Locate every uninfected red blood cell.
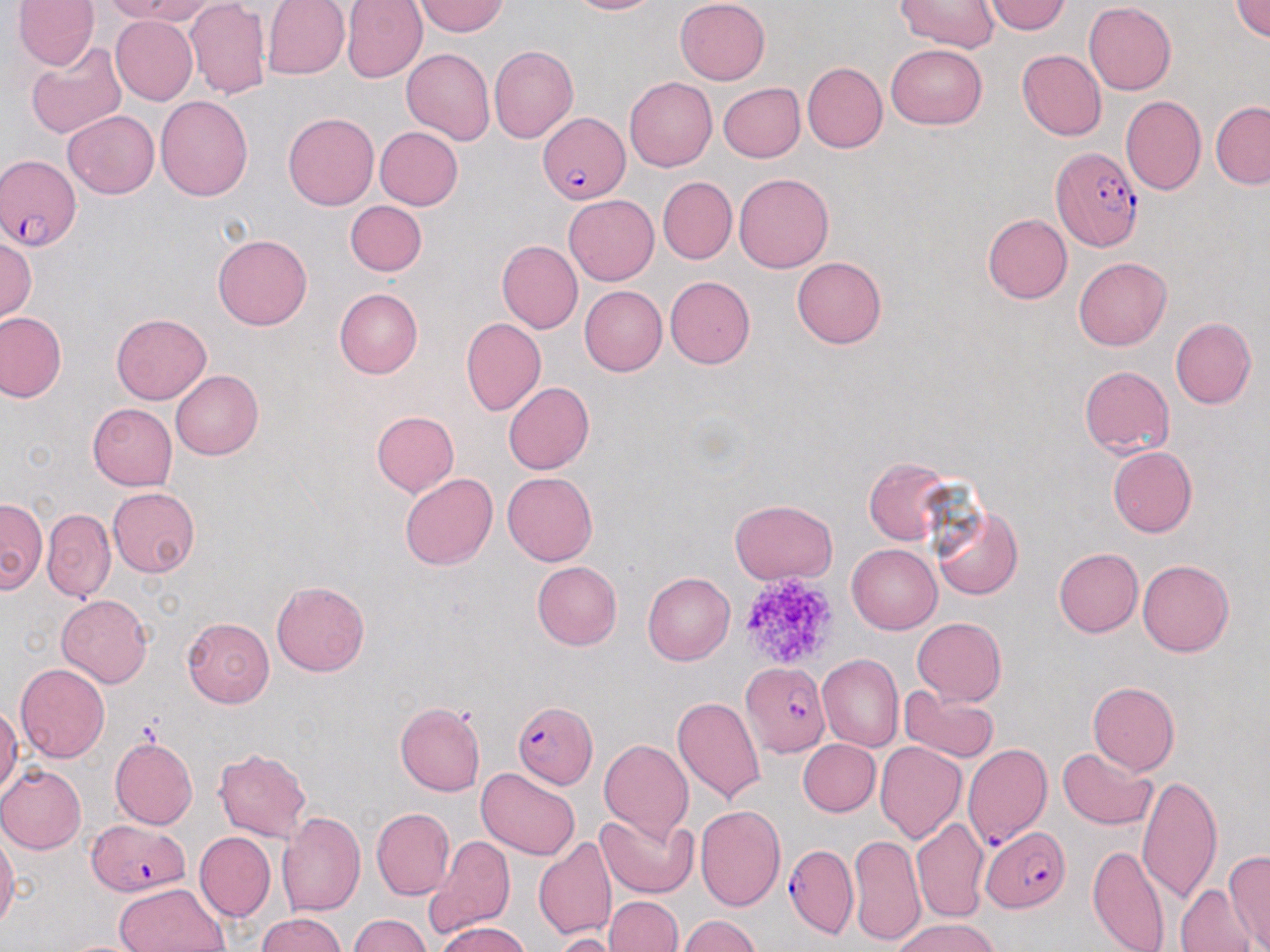
Approximate bounding boxes as (x1, y1, x2, y2) in pixels.
Uninfected red blood cells: (12, 0, 100, 69), (101, 0, 208, 24), (262, 0, 350, 80), (342, 0, 427, 83), (568, 0, 658, 15), (675, 0, 770, 85), (1232, 0, 1270, 42), (416, 1, 507, 36), (983, 1, 1072, 35), (1083, 1, 1176, 95), (184, 2, 271, 100), (896, 2, 999, 53), (110, 16, 198, 104), (24, 42, 127, 139), (885, 44, 988, 130), (489, 46, 578, 144), (401, 48, 495, 146), (1017, 50, 1107, 140), (802, 62, 887, 152), (624, 77, 717, 171), (718, 83, 805, 163), (156, 95, 252, 201), (1120, 96, 1206, 196), (1210, 102, 1270, 189), (62, 110, 159, 199), (283, 111, 378, 210), (374, 126, 463, 210), (734, 172, 834, 274), (657, 176, 736, 264), (564, 194, 658, 285), (345, 200, 426, 276), (982, 213, 1072, 304), (212, 234, 313, 330), (1, 236, 37, 323), (495, 240, 583, 333), (792, 256, 887, 348), (1073, 257, 1171, 350), (665, 276, 755, 369), (579, 285, 667, 375), (334, 288, 422, 378), (0, 311, 66, 402), (111, 313, 211, 405), (1170, 317, 1256, 409), (462, 318, 545, 416), (1079, 366, 1175, 457), (171, 370, 264, 460), (503, 382, 595, 475), (86, 403, 177, 492), (98, 404, 187, 575), (371, 411, 459, 497), (1108, 446, 1196, 538), (864, 456, 956, 544), (501, 471, 597, 566), (399, 472, 497, 570), (107, 487, 201, 578), (0, 498, 47, 593), (729, 499, 837, 583), (932, 504, 1023, 600), (43, 509, 115, 602), (847, 544, 941, 634), (1053, 548, 1143, 637), (1138, 558, 1235, 657), (532, 560, 622, 650), (642, 572, 733, 665), (272, 581, 370, 677), (57, 594, 152, 686), (182, 617, 275, 707), (912, 617, 1006, 705), (818, 653, 903, 752), (15, 663, 109, 763), (1087, 681, 1179, 774), (899, 686, 1000, 762), (672, 696, 767, 805), (395, 702, 486, 796), (1, 705, 21, 794), (110, 737, 198, 830), (598, 737, 694, 843), (798, 738, 880, 817), (875, 741, 967, 843), (1055, 747, 1158, 830), (214, 748, 311, 842), (0, 765, 87, 854), (476, 768, 581, 860), (1138, 774, 1224, 908), (693, 805, 786, 912), (371, 808, 455, 900), (276, 811, 366, 916), (596, 812, 698, 898), (910, 817, 989, 924), (195, 831, 274, 922), (0, 832, 20, 932), (848, 833, 924, 947), (424, 834, 516, 937), (534, 837, 617, 941), (1088, 844, 1173, 952), (1223, 849, 1270, 952), (112, 882, 228, 952), (1176, 882, 1255, 952), (605, 896, 682, 952), (258, 912, 345, 951), (349, 915, 430, 952), (677, 915, 761, 952), (892, 917, 1000, 952), (436, 921, 532, 952), (553, 932, 627, 952), (59, 939, 148, 952).

{
  "slide_level_diagnosis": "Plasmodium falciparum",
  "platelet_locations": "approximate bounding boxes as (x1, y1, x2, y2) in pixels: (741, 582, 840, 661)",
  "stain": "May-Grünwald-Giemsa",
  "preparation": "thin blood film",
  "field_of_view": "single",
  "magnification": "1000x",
  "plasmodium_falciparum_infected_red_blood_cell_locations": "approximate bounding boxes as (x1, y1, x2, y2) in pixels: (538, 110, 629, 205), (1049, 146, 1143, 251), (1, 154, 81, 250), (742, 662, 829, 756), (514, 701, 599, 787), (962, 745, 1053, 849), (87, 820, 189, 896), (980, 826, 1069, 912), (786, 844, 857, 938)",
  "modality": "light microscopy",
  "image_size": "1270×952 pixels"
}